Report the malaria status of this cell.
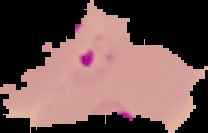
It is parasitized.

{
  "preparation": "thin blood smear",
  "image_type": "segmented cell region with the area outside set to black",
  "image_size": "208×133 pixels"
}